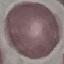

Malaria status: uninfected. Cell patch, automatically extracted from a larger field of view and resized to 64 × 64 pixels. Thin blood film. Giemsa stain. Acquired by smartphone through the microscope eyepiece.